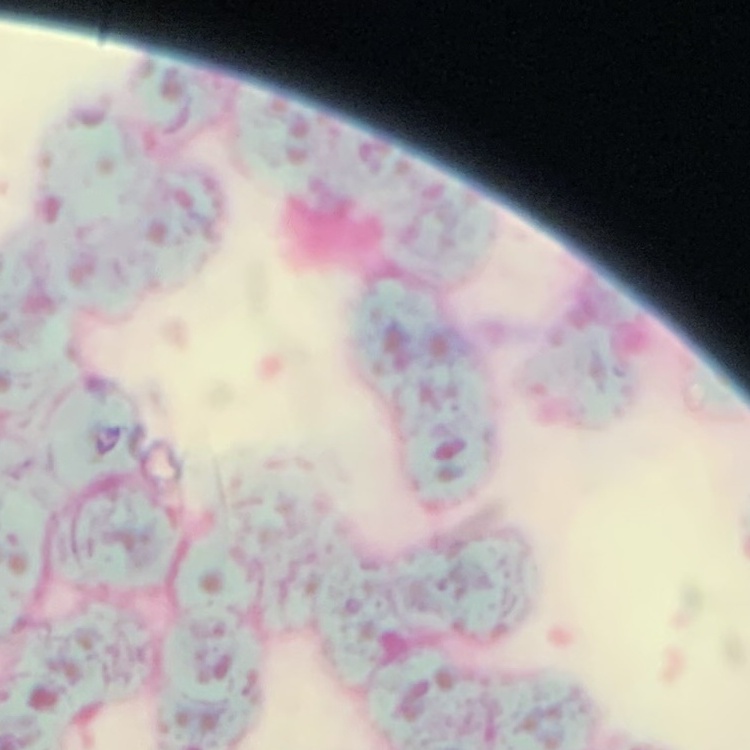
erythrocyte morphology = rouleaux formation
stain = Field's or Giemsa
preparation = thin blood film
image type = one tile cut from a larger photomicrograph